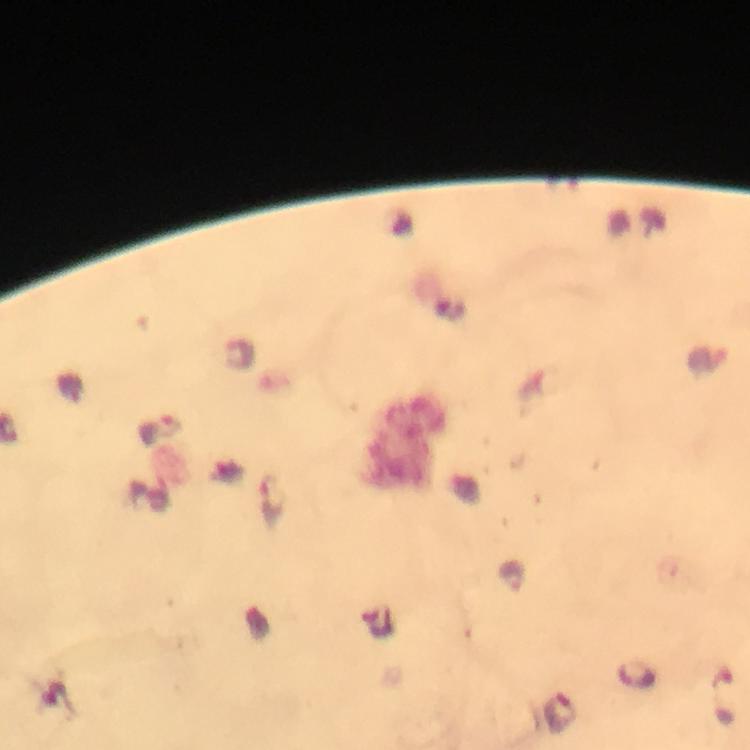

{
  "stain": "Giemsa",
  "image_size": "750×750 pixels",
  "context": "from a malaria diagnostic workup",
  "magnification": "100x",
  "immersion_oil": "applied",
  "capture": "smartphone mounted on the microscope",
  "preparation": "thick smear",
  "malaria_parasite_locations": "approximate centers as (x, y) in pixels: (171, 426), (273, 497), (721, 696)",
  "cropped_from": "one field of view"
}